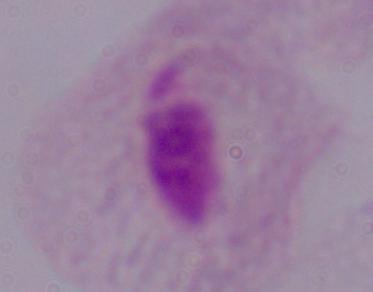

Summary:
  - Magnification: 1000x
  - Modality: micrograph
  - Identification: trichomonad